Classify this cell by malaria status.
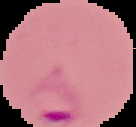

Parasitized.

image size = 136×127 pixels
image type = segmented cell region on a black background
preparation = thin blood smear